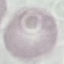

{
  "malaria_status": "uninfected",
  "stain": "Giemsa",
  "capture": "smartphone camera at the microscope eyepiece",
  "image_type": "cell patch, automatically extracted from a larger field of view and resized to 64 × 64 pixels",
  "preparation": "thin blood film"
}